Locate leukocytes (white blood cells).
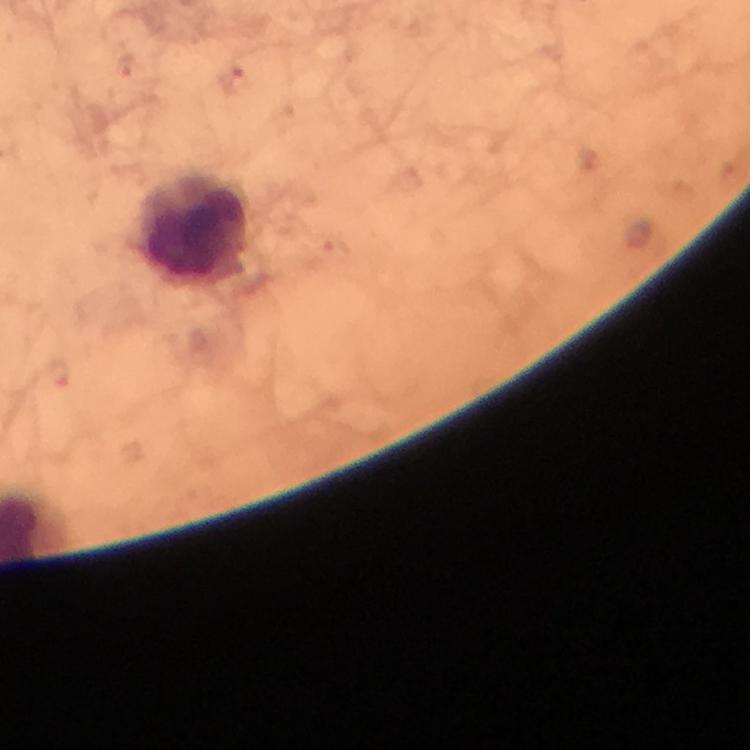

Approximate centers as {x, y} in pixels.
Leukocytes: {191, 232}.

Summary:
  - Plasmodium parasite locations: {125, 66}, {234, 78}
  - Image size: 750×750 pixels
  - Stain: Giemsa
  - Magnification: 100x
  - Capture: smartphone mounted on the microscope
  - Immersion oil: used
  - Cropped from: a single field of view
  - Context: from a malaria diagnostic workup
  - Preparation: thick blood smear